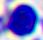

A leukocyte is seen. Captured at 400x magnification. Micrograph.